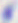 Toxoplasma gondii is shown. Captured at 400x magnification. Micrograph.